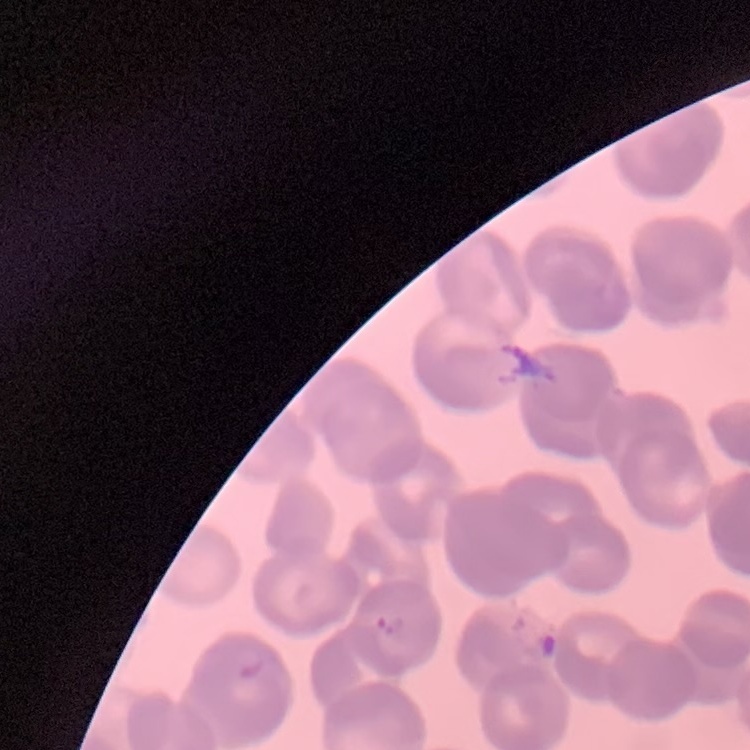
The red blood cells show rouleaux formation. Thin peripheral smear. Field's or Giemsa stain. Square crop of a larger photomicrograph.